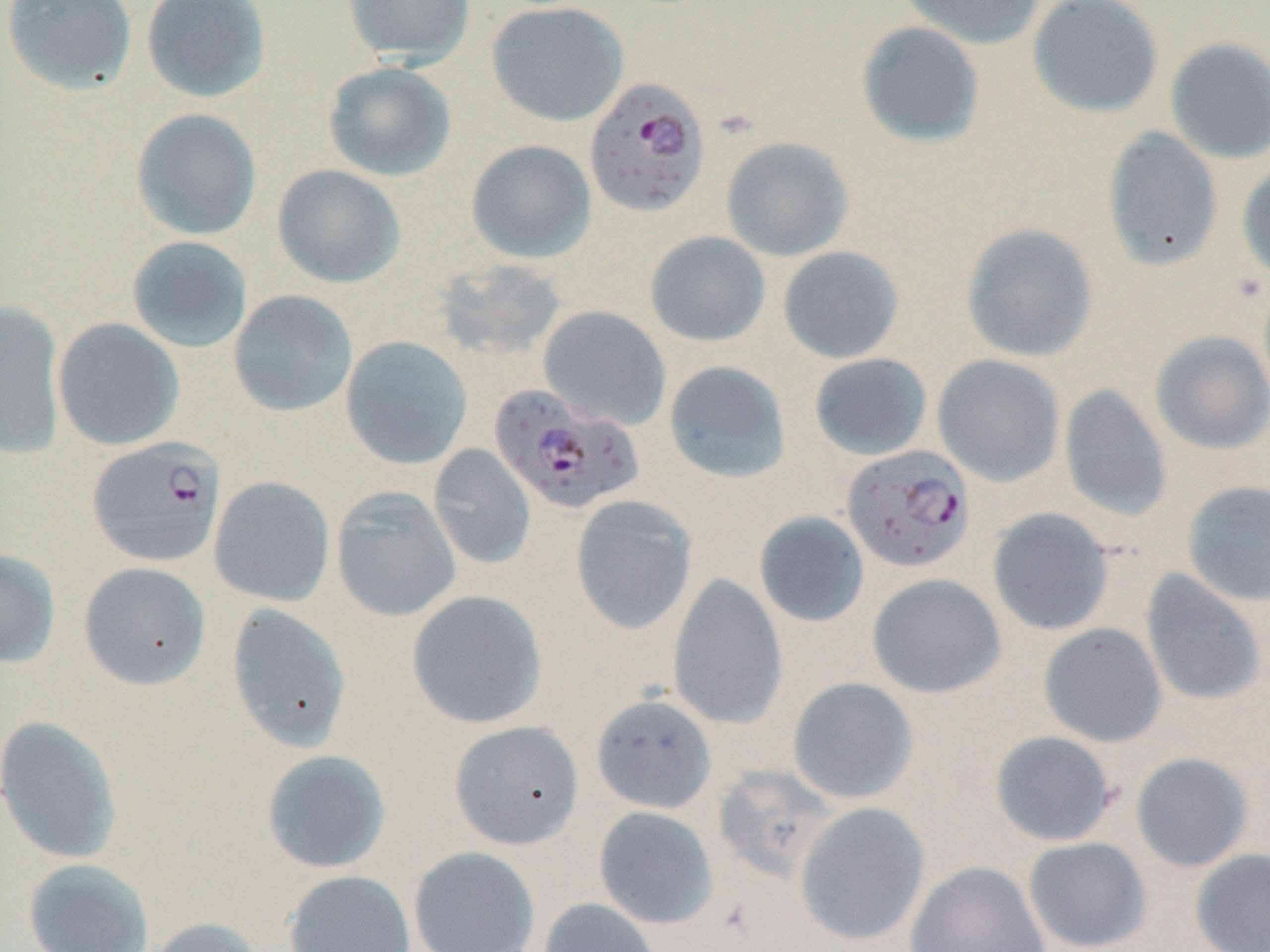

Approximate bounding boxes as [x1, y1, x2, y2] in pixels. Plasmodium falciparum-infected red blood cell locations: [585, 78, 710, 218], [489, 386, 645, 516], [87, 436, 226, 567], [842, 445, 975, 573]. Uninfected red blood cell locations: [2, 0, 137, 95], [141, 0, 271, 103], [341, 0, 475, 66], [895, 0, 1046, 51], [1027, 0, 1164, 118], [486, 2, 629, 127], [855, 20, 986, 147], [1165, 37, 1270, 164], [323, 62, 457, 182], [131, 108, 262, 240], [1103, 127, 1224, 272], [720, 136, 854, 262], [465, 139, 597, 263], [1237, 162, 1270, 283], [272, 164, 406, 288], [961, 223, 1098, 363], [645, 231, 770, 347], [126, 236, 253, 353], [778, 246, 904, 364], [433, 258, 568, 363], [228, 289, 357, 418], [0, 300, 66, 459], [538, 305, 671, 431], [53, 318, 185, 451], [1150, 330, 1270, 455], [341, 335, 473, 470], [809, 353, 932, 461], [932, 354, 1065, 486], [663, 360, 791, 484], [1059, 384, 1171, 522], [428, 445, 536, 570], [209, 476, 335, 607], [1182, 480, 1270, 607], [331, 486, 461, 622], [570, 495, 698, 635], [987, 507, 1114, 635], [754, 511, 870, 627], [0, 548, 61, 669], [78, 561, 211, 690], [1141, 568, 1266, 706], [668, 572, 787, 731], [867, 574, 1006, 699], [406, 590, 547, 729], [226, 603, 353, 752], [1038, 622, 1167, 747], [787, 677, 919, 804], [591, 694, 717, 814], [0, 715, 123, 864], [449, 720, 584, 850], [989, 730, 1118, 847], [261, 749, 391, 873], [1130, 752, 1255, 873], [711, 764, 841, 885], [794, 801, 929, 946], [593, 805, 719, 929], [1022, 837, 1152, 951], [408, 846, 540, 952], [1190, 848, 1270, 952], [23, 857, 154, 952], [906, 860, 1050, 952], [283, 870, 416, 952], [538, 897, 663, 952], [144, 916, 266, 952]. Slide-level diagnosis: Plasmodium falciparum. May-Grünwald-Giemsa stain. Thin blood smear. 1000x magnification. Image is 1270×952 pixels. Single field of view. Light microscopy.